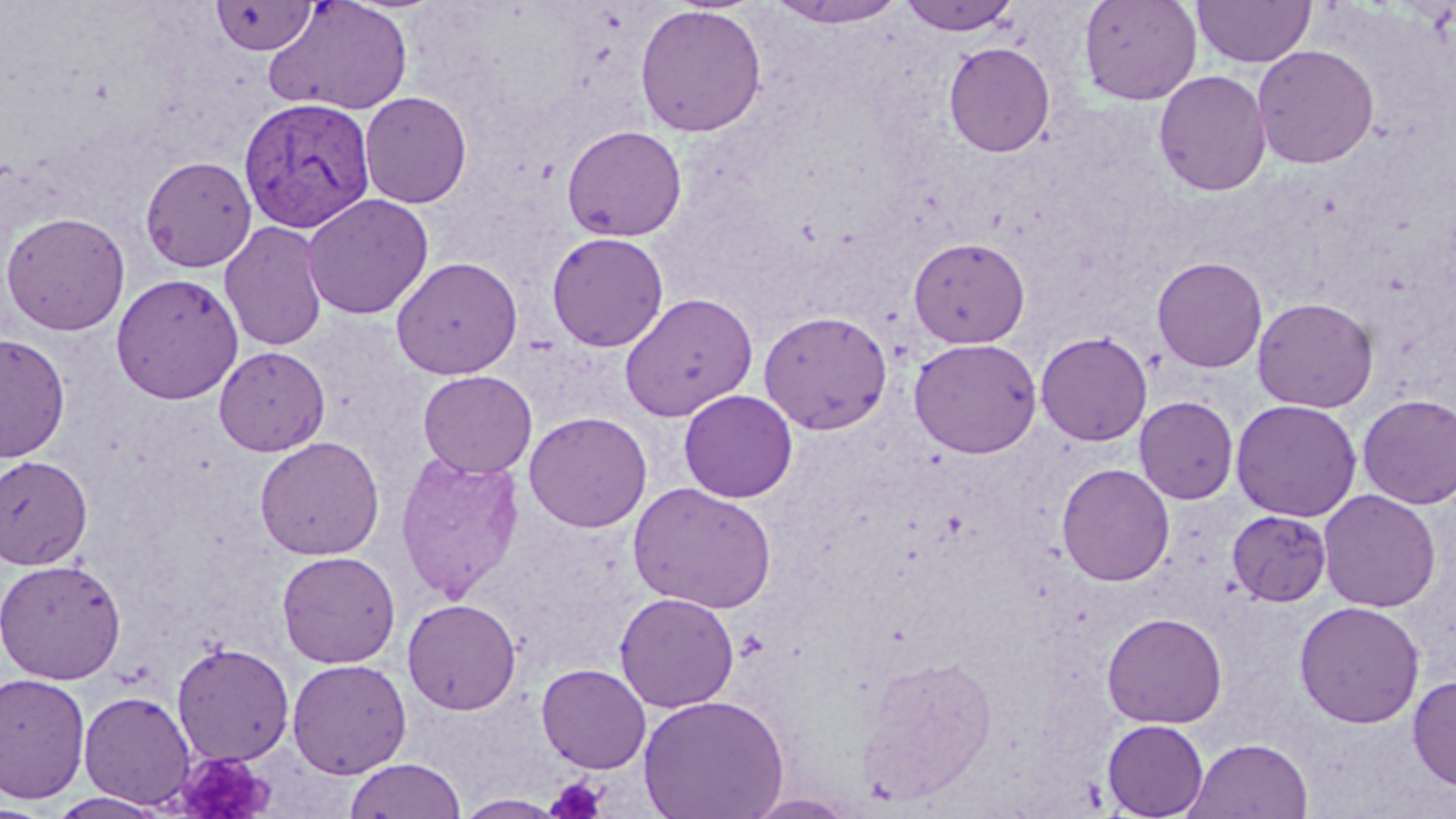
Approximate bounding boxes as named x1/y1/x2/y2 corners in pixels. Plasmodium vivax-infected red blood cell locations: (x1=240, y1=96, x2=379, y2=234). Platelet locations: (x1=172, y1=751, x2=276, y2=819), (x1=546, y1=776, x2=608, y2=819). Uninfected red blood cell locations: (x1=898, y1=0, x2=1023, y2=36), (x1=1079, y1=0, x2=1202, y2=105), (x1=1192, y1=0, x2=1315, y2=68), (x1=210, y1=1, x2=319, y2=55), (x1=264, y1=1, x2=413, y2=116), (x1=766, y1=1, x2=911, y2=28), (x1=634, y1=4, x2=767, y2=137), (x1=943, y1=42, x2=1056, y2=157), (x1=1252, y1=44, x2=1379, y2=169), (x1=1154, y1=70, x2=1272, y2=196), (x1=359, y1=91, x2=472, y2=208), (x1=561, y1=125, x2=687, y2=242), (x1=140, y1=155, x2=257, y2=272), (x1=301, y1=193, x2=434, y2=320), (x1=1, y1=212, x2=130, y2=335), (x1=220, y1=220, x2=328, y2=352), (x1=546, y1=232, x2=668, y2=351), (x1=908, y1=237, x2=1031, y2=348), (x1=391, y1=256, x2=523, y2=379), (x1=1152, y1=256, x2=1268, y2=373), (x1=111, y1=273, x2=243, y2=404), (x1=619, y1=293, x2=758, y2=421), (x1=1252, y1=297, x2=1379, y2=413), (x1=759, y1=310, x2=893, y2=434), (x1=1036, y1=330, x2=1153, y2=446), (x1=0, y1=333, x2=71, y2=462), (x1=909, y1=337, x2=1043, y2=458), (x1=214, y1=346, x2=329, y2=455), (x1=418, y1=369, x2=537, y2=478), (x1=679, y1=389, x2=798, y2=503), (x1=1357, y1=393, x2=1456, y2=509), (x1=1134, y1=396, x2=1239, y2=504), (x1=1230, y1=399, x2=1362, y2=521), (x1=524, y1=411, x2=652, y2=532), (x1=255, y1=436, x2=385, y2=560), (x1=395, y1=449, x2=526, y2=603), (x1=0, y1=455, x2=93, y2=569), (x1=1056, y1=463, x2=1175, y2=586), (x1=628, y1=481, x2=777, y2=614), (x1=1318, y1=489, x2=1442, y2=613), (x1=1227, y1=509, x2=1332, y2=607), (x1=276, y1=550, x2=401, y2=668), (x1=0, y1=558, x2=127, y2=684), (x1=614, y1=591, x2=740, y2=712), (x1=402, y1=598, x2=522, y2=714), (x1=1294, y1=601, x2=1425, y2=728), (x1=1101, y1=611, x2=1228, y2=728), (x1=172, y1=641, x2=295, y2=766), (x1=860, y1=654, x2=997, y2=805), (x1=287, y1=658, x2=412, y2=779), (x1=536, y1=663, x2=651, y2=774), (x1=0, y1=672, x2=91, y2=804), (x1=1408, y1=674, x2=1456, y2=792), (x1=78, y1=690, x2=196, y2=809), (x1=638, y1=694, x2=789, y2=819), (x1=1101, y1=719, x2=1209, y2=818), (x1=1185, y1=737, x2=1313, y2=819), (x1=343, y1=757, x2=467, y2=818), (x1=46, y1=792, x2=170, y2=819), (x1=744, y1=793, x2=860, y2=818), (x1=454, y1=794, x2=569, y2=818). Slide-level diagnosis: Plasmodium vivax. May-Grünwald-Giemsa stain. Captured at 1000x magnification. Light microscopy. Image is 1456×819 pixels. One field of a larger specimen. Thin blood film.